Identify the parasite.
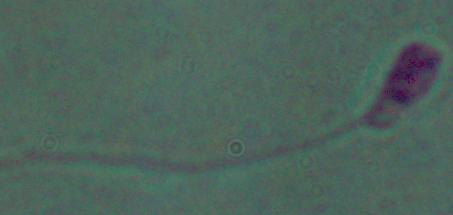
Leishmania.

Summary:
  - Modality: micrograph
  - Magnification: 1000x